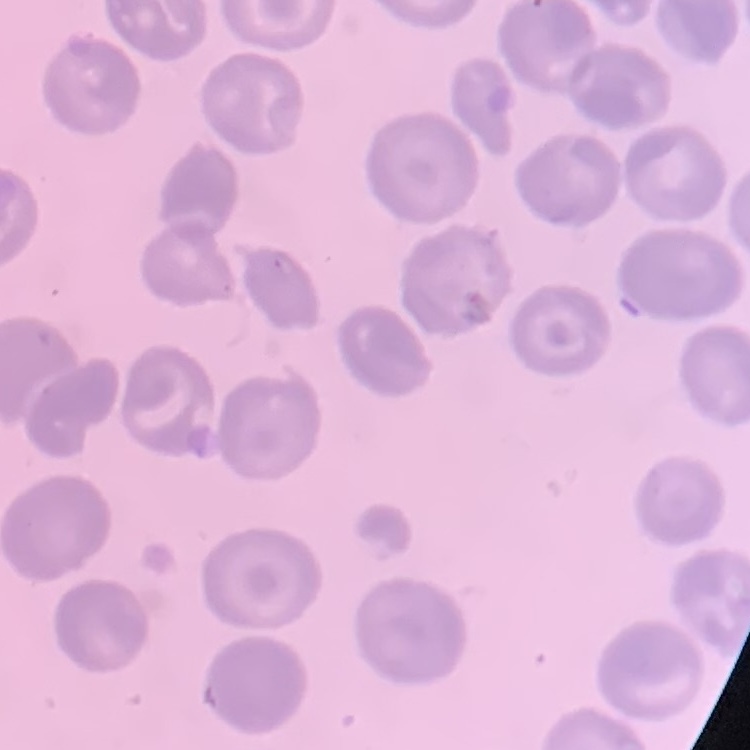
{
  "red_blood_cell_morphology": "no rouleaux formation",
  "stain": "Field's or Giemsa",
  "image_type": "one tile cut from a larger photomicrograph",
  "preparation": "thin blood smear"
}